Give the preparation type.
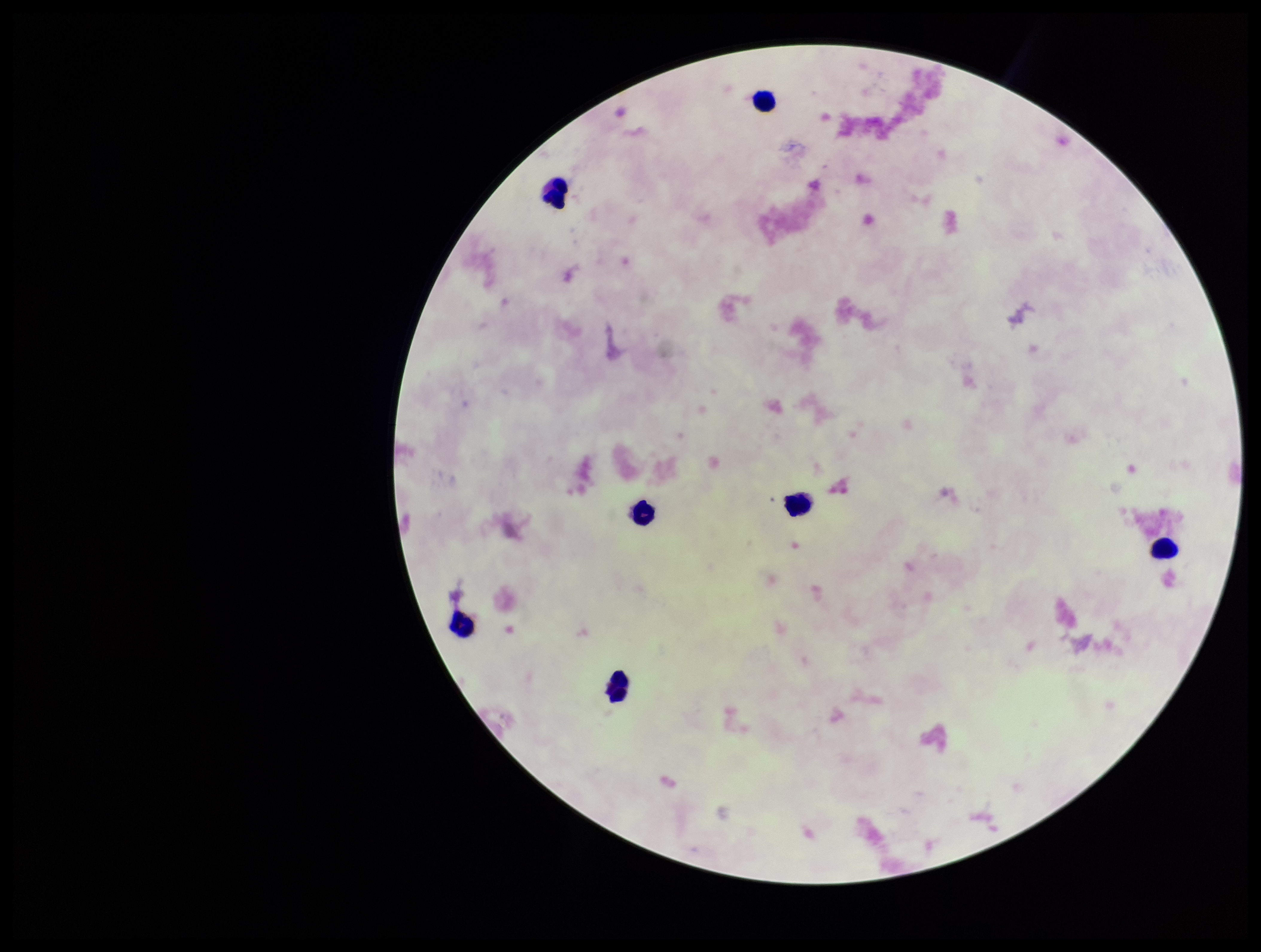

It is a thick blood smear.

Summary:
  - Plasmodium parasites: none seen
  - Capture: smartphone photograph through the microscope eyepiece
  - Field of view: one from this slide
  - Image size: 1261×952 pixels
  - Leukocyte count: 7
  - Stain: Giemsa
  - Parasite count: 0
  - Patient malaria status: negative